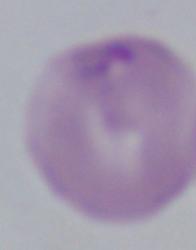

A Babesia parasite is shown. Captured at 1000x magnification. Micrograph.